Classify this cell by malaria status.
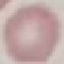

Uninfected.

Giemsa-stained preparation. Thin blood smear. Cell patch, automatically extracted from a larger field of view and resized to 64 × 64 pixels. Acquired by smartphone through the microscope eyepiece.